Locate every blood parasite and identify its species.
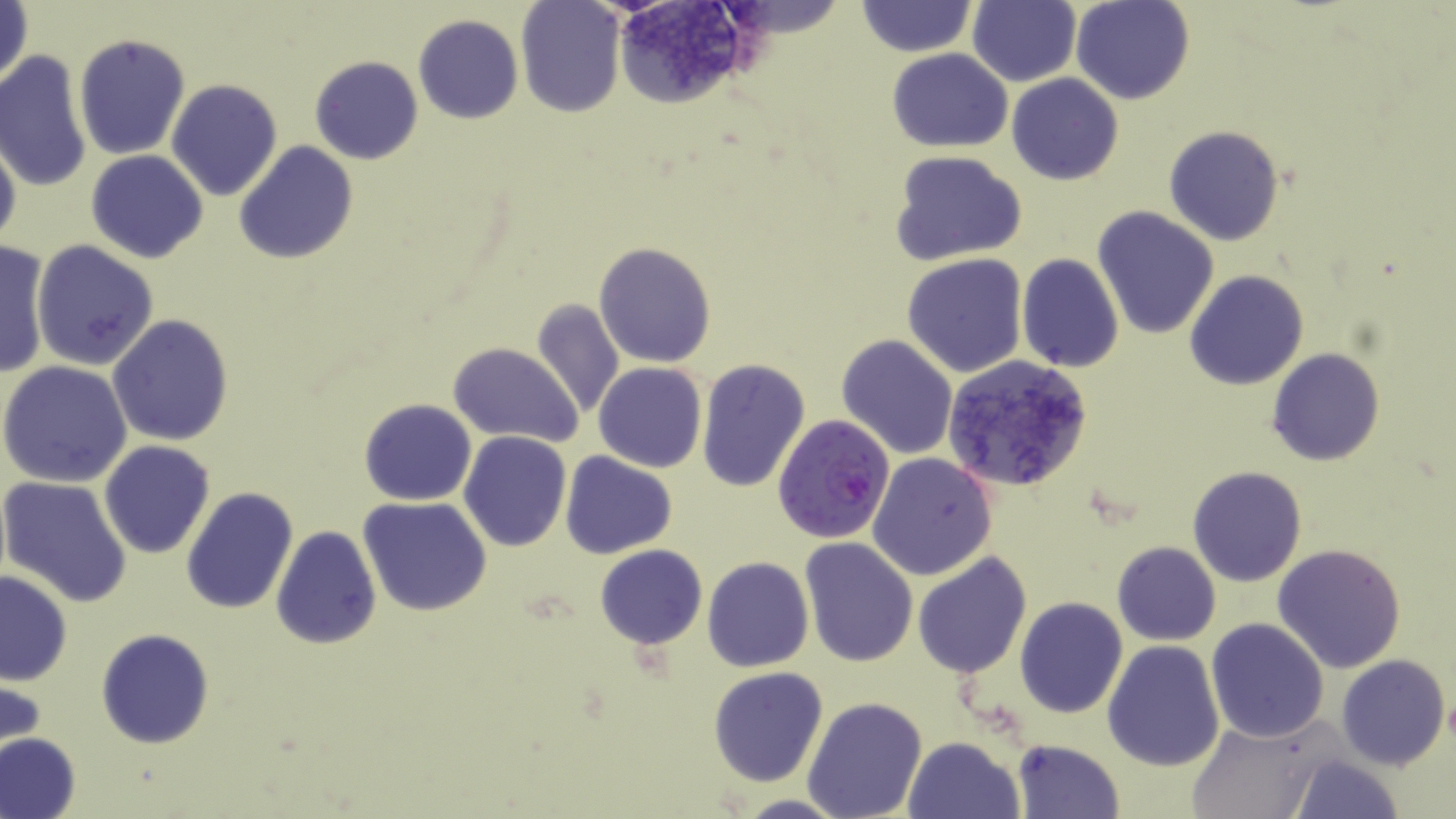

Approximate bounding boxes as named x1/y1/x2/y2 corners in pixels.
Plasmodium falciparum-infected red blood cells: (x1=771, y1=412, x2=895, y2=542).
No Plasmodium ovale, Plasmodium malariae, Plasmodium vivax, Babesia divergens, or Trypanosoma brucei observed.

Uninfected red blood cell locations: (x1=605, y1=0, x2=761, y2=109), (x1=969, y1=0, x2=1081, y2=87), (x1=1072, y1=0, x2=1194, y2=105), (x1=856, y1=1, x2=975, y2=57), (x1=1, y1=2, x2=33, y2=94), (x1=514, y1=2, x2=624, y2=117), (x1=413, y1=15, x2=524, y2=123), (x1=73, y1=33, x2=190, y2=161), (x1=887, y1=47, x2=1013, y2=153), (x1=0, y1=50, x2=92, y2=194), (x1=310, y1=56, x2=423, y2=165), (x1=1006, y1=73, x2=1123, y2=185), (x1=166, y1=80, x2=282, y2=201), (x1=1163, y1=126, x2=1286, y2=246), (x1=0, y1=127, x2=22, y2=256), (x1=233, y1=142, x2=358, y2=264), (x1=85, y1=149, x2=209, y2=264), (x1=889, y1=150, x2=1027, y2=265), (x1=1092, y1=207, x2=1219, y2=339), (x1=31, y1=239, x2=159, y2=370), (x1=594, y1=241, x2=717, y2=367), (x1=0, y1=242, x2=52, y2=380), (x1=902, y1=253, x2=1029, y2=377), (x1=1017, y1=255, x2=1124, y2=372), (x1=1184, y1=271, x2=1308, y2=390), (x1=531, y1=297, x2=627, y2=422), (x1=107, y1=316, x2=233, y2=446), (x1=837, y1=334, x2=958, y2=459), (x1=449, y1=342, x2=583, y2=447), (x1=1266, y1=349, x2=1384, y2=465), (x1=944, y1=355, x2=1094, y2=493), (x1=695, y1=359, x2=811, y2=492), (x1=0, y1=360, x2=133, y2=487), (x1=594, y1=362, x2=707, y2=473), (x1=359, y1=398, x2=477, y2=505), (x1=459, y1=431, x2=570, y2=551), (x1=98, y1=440, x2=215, y2=558), (x1=559, y1=451, x2=678, y2=559), (x1=867, y1=453, x2=998, y2=581), (x1=1186, y1=466, x2=1307, y2=586), (x1=1, y1=476, x2=134, y2=608), (x1=180, y1=488, x2=299, y2=614), (x1=359, y1=497, x2=492, y2=617), (x1=270, y1=524, x2=381, y2=650), (x1=799, y1=537, x2=920, y2=667), (x1=1111, y1=541, x2=1221, y2=645), (x1=1272, y1=543, x2=1406, y2=673), (x1=594, y1=544, x2=707, y2=649), (x1=911, y1=551, x2=1033, y2=680), (x1=702, y1=557, x2=814, y2=672), (x1=0, y1=571, x2=72, y2=687), (x1=1014, y1=598, x2=1128, y2=718), (x1=1205, y1=617, x2=1329, y2=741), (x1=96, y1=628, x2=214, y2=748), (x1=1101, y1=639, x2=1224, y2=771), (x1=1335, y1=653, x2=1450, y2=771), (x1=708, y1=666, x2=829, y2=787), (x1=1, y1=674, x2=46, y2=765), (x1=803, y1=697, x2=928, y2=819), (x1=1186, y1=716, x2=1332, y2=819), (x1=0, y1=733, x2=82, y2=819), (x1=904, y1=736, x2=1024, y2=819), (x1=1012, y1=739, x2=1125, y2=818), (x1=1287, y1=754, x2=1405, y2=819), (x1=732, y1=794, x2=855, y2=818). Slide-level diagnosis: Plasmodium falciparum. One field of a larger specimen. Optical microscopy. Image is 1456×819 pixels. Thin blood smear. 1000x magnification. May-Grünwald-Giemsa-stained preparation.